Locate every blood parasite and identify its species.
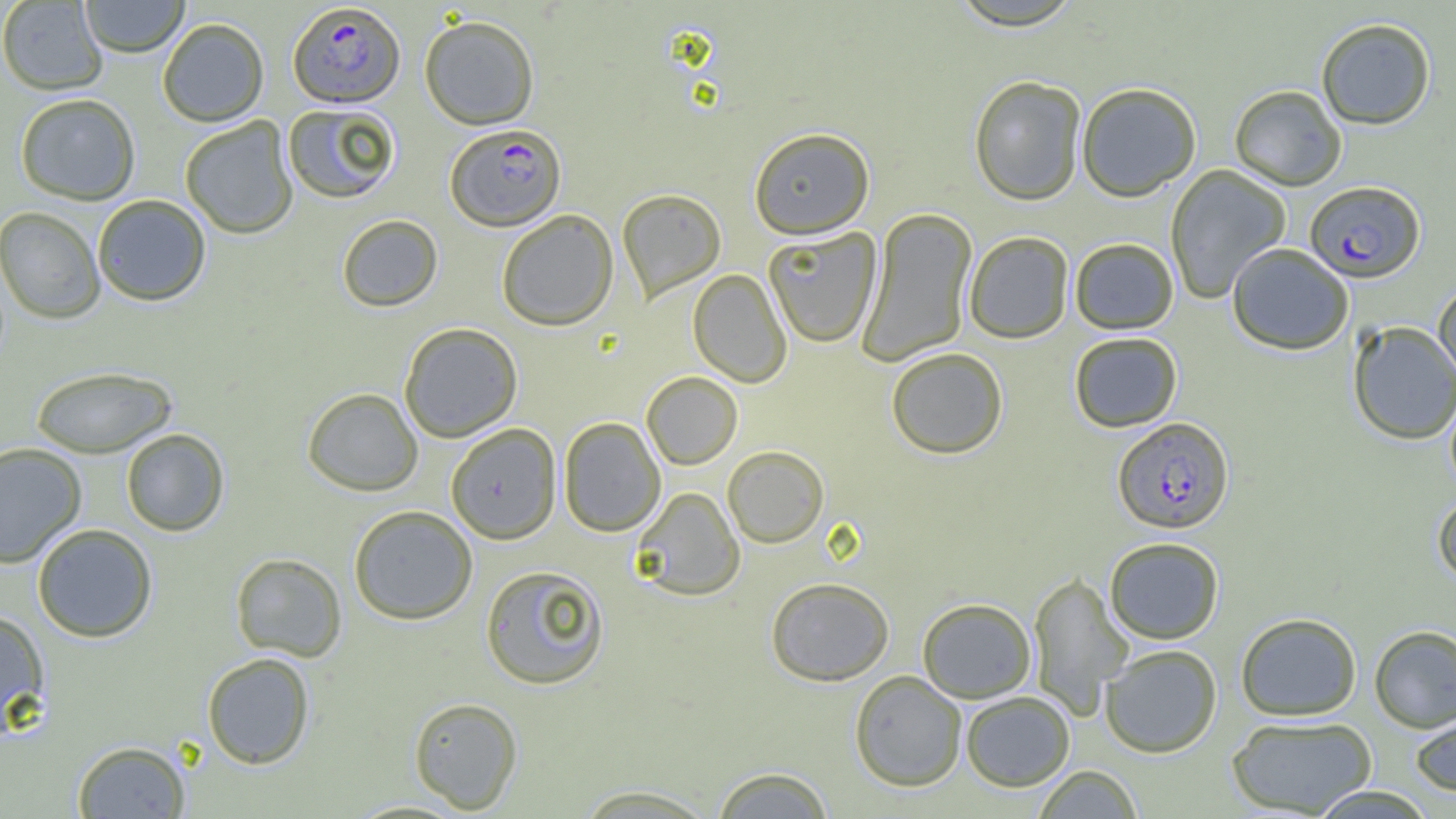
Approximate bounding boxes as [x1, y1, x2, y2] in pixels.
Plasmodium falciparum-infected red blood cells: [288, 2, 405, 107], [444, 123, 566, 231], [1304, 181, 1425, 284], [1111, 417, 1235, 534].
No Plasmodium ovale, Plasmodium malariae, Plasmodium vivax, Babesia divergens, or Trypanosoma brucei observed.

Uninfected red blood cell locations: [80, 0, 189, 58], [1, 1, 108, 96], [947, 1, 1086, 32], [419, 14, 539, 129], [157, 17, 269, 127], [1316, 17, 1436, 130], [968, 75, 1087, 206], [1076, 83, 1201, 202], [1229, 85, 1347, 191], [14, 93, 141, 205], [282, 102, 401, 204], [180, 117, 298, 239], [749, 127, 875, 239], [1165, 164, 1291, 304], [616, 188, 726, 304], [91, 194, 211, 306], [0, 206, 106, 324], [857, 207, 977, 367], [496, 209, 618, 331], [337, 214, 443, 312], [763, 228, 881, 348], [964, 232, 1074, 344], [1070, 238, 1179, 334], [1227, 243, 1354, 356], [688, 268, 792, 388], [1433, 282, 1456, 387], [1348, 321, 1456, 445], [399, 322, 523, 442], [1069, 332, 1183, 433], [886, 347, 1008, 459], [30, 365, 177, 458], [641, 372, 743, 470], [1445, 386, 1456, 497], [302, 387, 424, 496], [558, 417, 666, 536], [445, 424, 561, 544], [120, 428, 230, 536], [0, 442, 86, 567], [722, 445, 829, 548], [631, 487, 745, 601], [1432, 492, 1456, 588], [348, 505, 478, 625], [32, 523, 158, 643], [1104, 537, 1225, 644], [230, 552, 347, 661], [480, 564, 610, 690], [1027, 571, 1133, 718], [765, 577, 894, 685], [917, 598, 1037, 703], [0, 609, 51, 737], [1235, 612, 1362, 721], [1369, 625, 1456, 733], [1099, 644, 1223, 757], [201, 652, 315, 769], [849, 670, 967, 791], [960, 691, 1075, 791], [408, 696, 523, 814], [1409, 706, 1456, 796], [1226, 716, 1378, 817], [72, 740, 191, 818], [710, 765, 835, 819], [1033, 765, 1142, 818], [570, 784, 721, 818], [1307, 785, 1439, 819]. Slide-level diagnosis: Plasmodium falciparum. Thin blood film. Image is 1456×819 pixels. One field of a larger specimen. Optical microscopy. 1000x magnification.